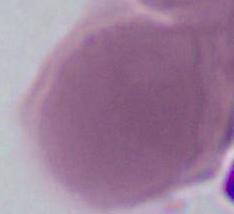

An erythrocyte is shown. Micrograph. Captured at 1000x magnification.